State which cell type is depicted.
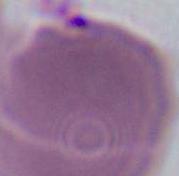

An erythrocyte.

magnification: 1000x
modality: photomicrograph